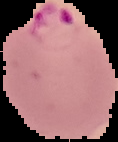
image type = cell region segmented out of the field of view; surrounding area masked to black
result = Plasmodium parasites identified
preparation = thin blood smear
image size = 118×142 pixels